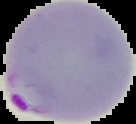
image type = segmented cell region on a black background
image size = 136×124 pixels
result = malaria parasites detected
preparation = thin blood film